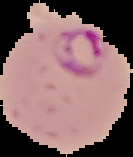

preparation = thin blood smear
malaria status = parasitized
image type = segmented cell region with the area outside set to black
image size = 133×157 pixels